Assess this cell for malaria.
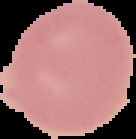

Uninfected.

image size = 136×139 pixels
preparation = thin blood smear
image type = segmented cell region on a black background